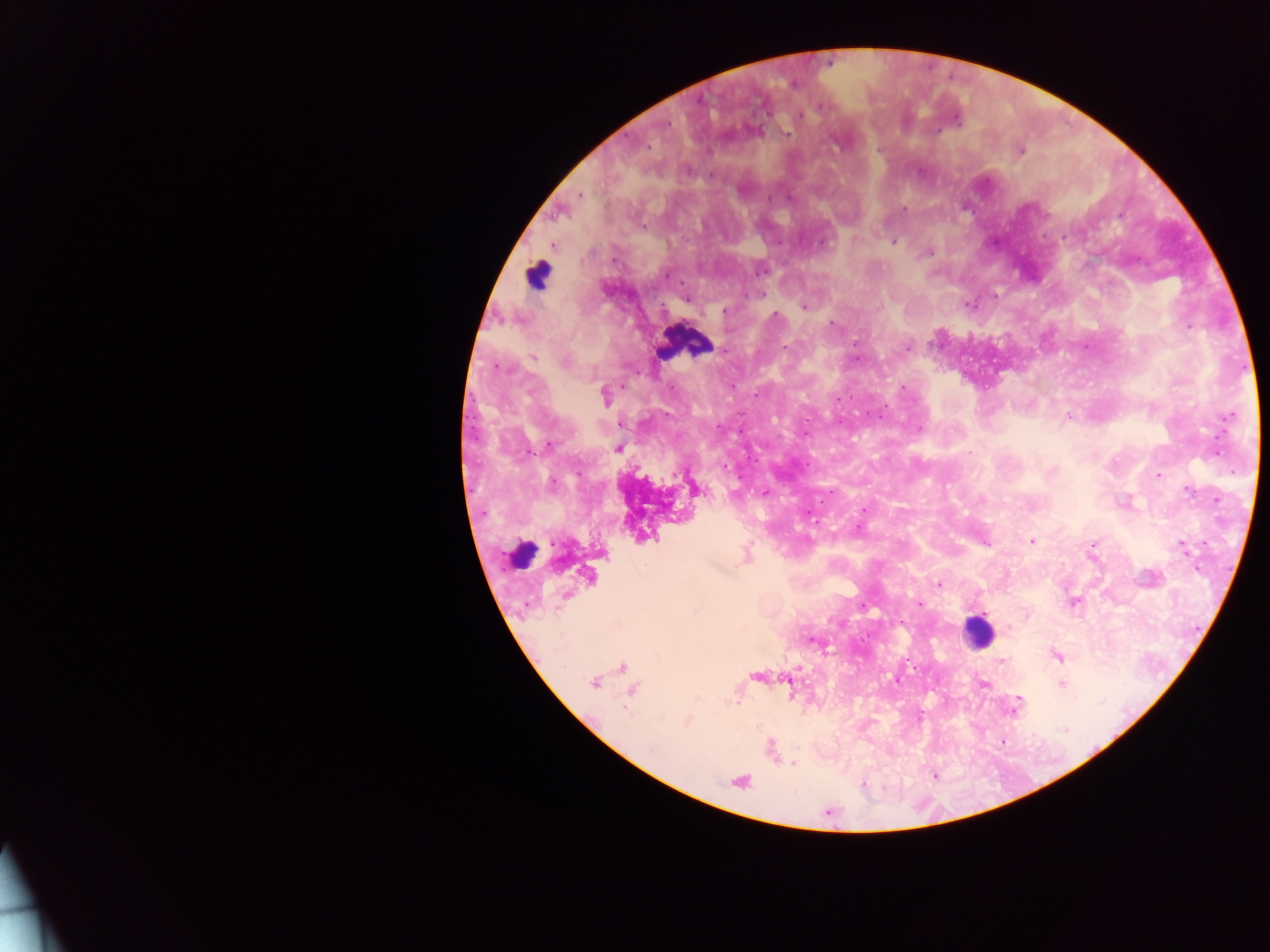

malaria parasite locations = approximate centers as (x, y) in pixels: (793, 84), (821, 106), (799, 116), (956, 119), (668, 125), (786, 134), (648, 146), (1021, 151), (711, 175), (580, 195), (790, 197), (769, 198), (904, 209), (644, 227), (1063, 238), (821, 242), (894, 242), (554, 245), (929, 253), (760, 272), (763, 295), (995, 295), (685, 300), (969, 305), (804, 307), (725, 311), (775, 314), (831, 322), (1189, 326), (856, 343), (785, 348), (907, 348), (724, 350), (532, 358), (857, 358), (500, 367), (903, 387), (757, 394), (604, 396), (838, 399), (879, 416), (1068, 416), (1230, 416), (621, 425), (717, 427), (919, 429), (548, 445), (618, 448), (724, 465), (674, 475), (1158, 475), (552, 483), (1188, 491), (764, 492), (864, 510), (1033, 541), (985, 543), (1093, 544), (1182, 547), (939, 584), (1073, 602), (919, 604), (863, 606), (1009, 628), (811, 641), (1057, 657), (1001, 660), (593, 683), (983, 684), (1062, 684), (735, 704), (1016, 707), (687, 722), (1066, 730), (793, 763), (863, 784)
country = Ghana
leukocyte locations = approximate centers as (x, y) in pixels: (537, 275), (685, 343), (521, 547), (977, 631)
capture = mobile-phone photograph through a microscope
preparation = thick blood film
image size = 1270×952 pixels
field of view = single